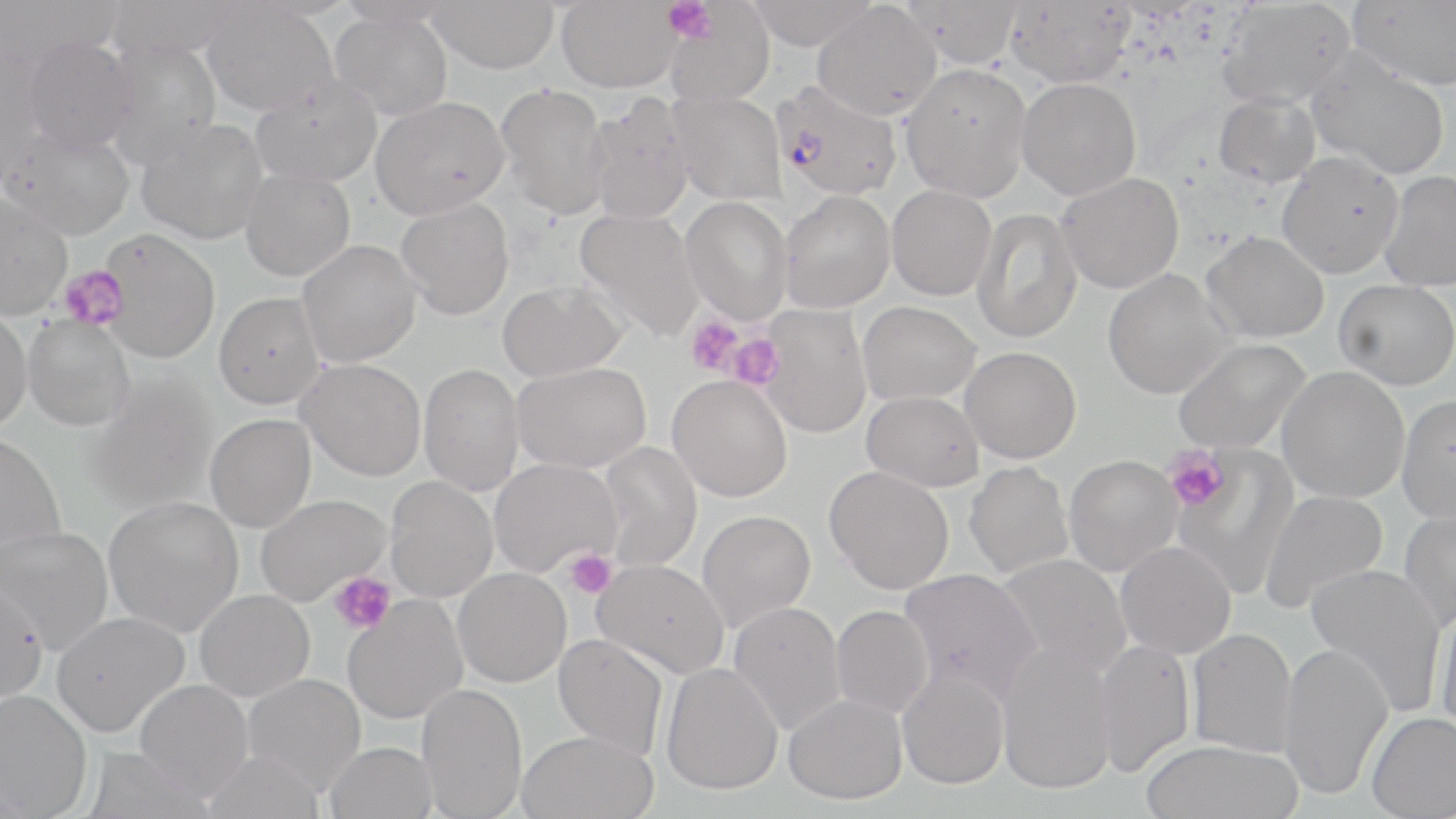

slide-level diagnosis = Plasmodium falciparum
platelet locations = approximate bounding boxes as (x1,y1)-(x2,y2) corner pairs in pixels: (662,0)-(715,42), (58,265)-(129,330), (686,313)-(745,377), (727,333)-(784,390), (1164,447)-(1231,512), (564,548)-(617,599), (330,571)-(396,635)
field of view = one of a larger specimen
stain = May-Grünwald-Giemsa
magnification = 1000x
modality = optical microscopy
preparation = thin blood smear
Plasmodium falciparum-infected red blood cell locations = approximate bounding boxes as (x1,y1)-(x2,y2) corner pairs in pixels: (772,83)-(908,201)
uninfected red blood cell locations = approximate bounding boxes as (x1,y1)-(x2,y2) corner pairs in pixels: (0,0)-(125,68), (427,0)-(559,74), (555,0)-(681,93), (746,0)-(879,50), (1348,0)-(1456,90), (107,1)-(243,60), (334,1)-(457,29), (903,1)-(1024,69), (1003,1)-(1136,88), (1215,1)-(1355,110), (201,2)-(338,116), (812,2)-(941,120), (665,3)-(775,106), (330,9)-(453,120), (21,37)-(137,153), (104,39)-(222,166), (1303,46)-(1452,181), (900,62)-(1032,202), (250,77)-(382,187), (1016,78)-(1141,200), (495,83)-(611,218), (667,90)-(785,205), (1213,93)-(1321,189), (370,95)-(510,219), (584,95)-(694,225), (135,117)-(268,244), (1,122)-(136,239), (1275,151)-(1404,278), (240,168)-(355,281), (1378,170)-(1456,291), (1057,172)-(1184,293), (886,185)-(996,301), (779,190)-(895,312), (1,193)-(73,319), (680,196)-(793,324), (395,197)-(514,320), (574,207)-(704,343), (971,208)-(1083,344), (98,228)-(220,362), (1201,231)-(1329,343), (296,240)-(421,368), (1102,268)-(1231,398), (1333,279)-(1456,390), (497,280)-(626,382), (213,292)-(325,408), (858,301)-(981,405), (757,304)-(873,437), (0,306)-(32,432), (24,315)-(134,431), (1173,338)-(1310,453), (960,346)-(1081,463), (297,357)-(426,481), (512,362)-(651,473), (419,363)-(525,496), (1277,365)-(1410,503), (85,374)-(219,515), (667,375)-(792,501), (862,390)-(984,491), (1396,395)-(1456,523), (205,414)-(315,532), (0,432)-(65,556), (597,441)-(702,572), (1173,448)-(1296,599), (1063,455)-(1182,576), (489,458)-(621,577), (964,462)-(1073,578), (824,466)-(954,594), (385,476)-(498,602), (1258,490)-(1388,611), (255,494)-(390,605), (103,496)-(243,637), (1399,507)-(1456,631), (697,510)-(816,632), (0,525)-(114,653), (1115,541)-(1236,659), (995,554)-(1131,677), (593,559)-(730,679), (1303,562)-(1448,716), (453,567)-(571,687), (899,568)-(1042,702), (0,580)-(48,704), (194,589)-(315,701), (342,595)-(468,724), (729,602)-(845,734), (1433,603)-(1456,744), (831,605)-(934,717), (51,611)-(189,736), (1186,628)-(1297,758), (553,634)-(669,760), (1092,639)-(1194,777), (997,641)-(1118,794), (1277,642)-(1394,800), (661,662)-(783,795), (898,667)-(1009,789), (242,674)-(365,795), (134,679)-(253,799), (416,683)-(527,818), (0,688)-(93,817), (783,693)-(908,805), (1365,712)-(1456,819), (517,730)-(658,819), (1139,739)-(1303,819), (325,741)-(437,819), (203,749)-(325,818)
image size = 1456×819 pixels